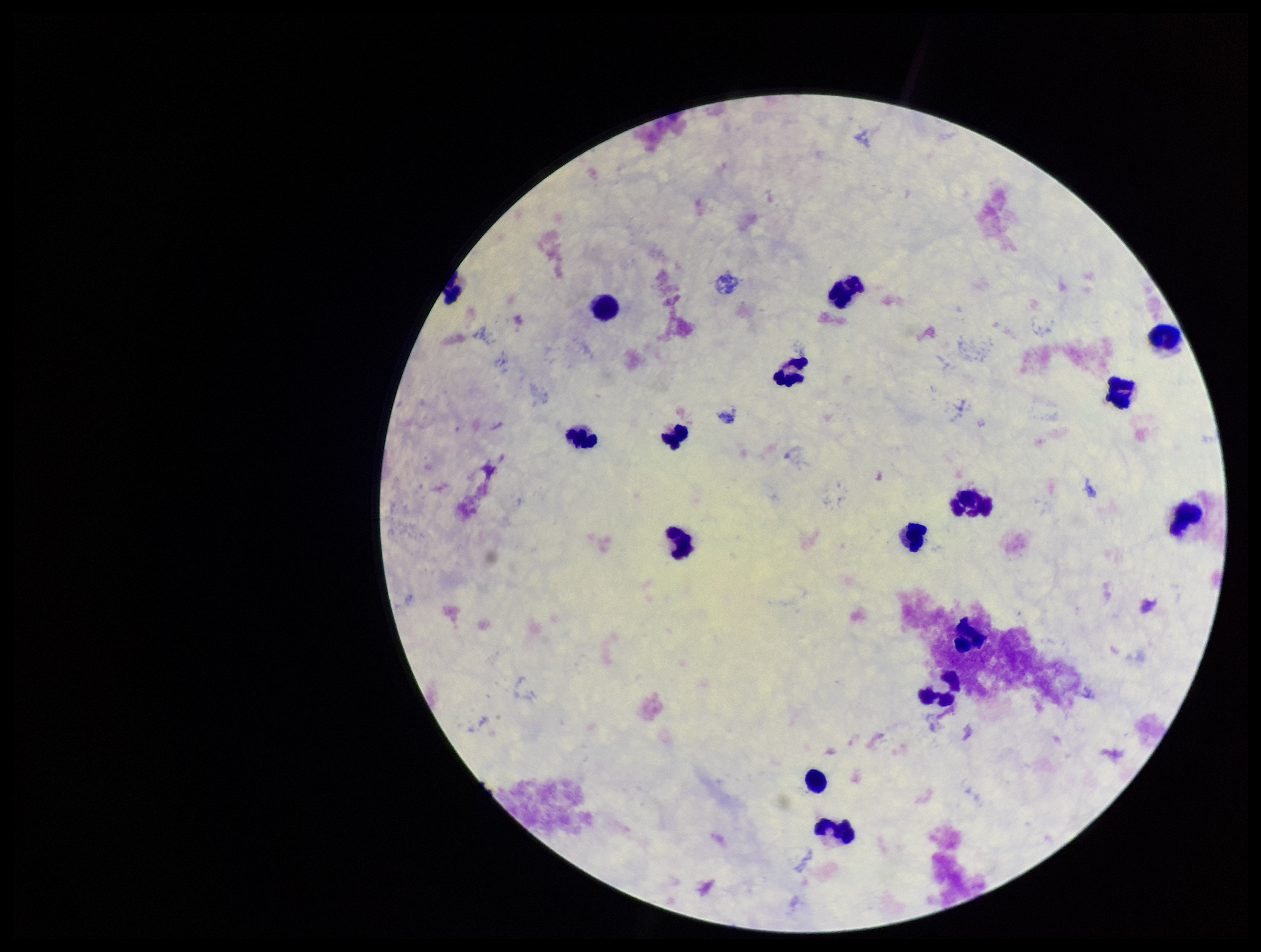

{
  "plasmodium_parasites": "none seen",
  "stain": "Giemsa",
  "leukocyte_count": 16,
  "capture": "smartphone photograph through the microscope eyepiece",
  "preparation": "thick blood smear",
  "parasite_count": 0,
  "patient_malaria_status": "negative",
  "field_of_view": "one from this slide",
  "image_size": "1261×952 pixels"
}